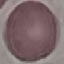

Summary:
  - Malaria status: uninfected
  - Image type: cell patch, automatically extracted from a larger field of view and resized to 64 × 64 pixels
  - Capture: smartphone through the microscope eyepiece
  - Stain: Giemsa
  - Preparation: thin smear